Classify this cell by malaria status.
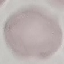
It is uninfected.

Summary:
  - Image type: automatically extracted cell patch, resized to 64 × 64 pixels
  - Stain: Giemsa
  - Preparation: thin smear
  - Capture: smartphone through the microscope eyepiece